Classify this cell by malaria status.
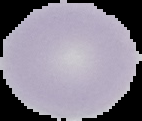
Uninfected.

Image is 142×121 pixels. From a thin blood smear. Cell region segmented out of the field of view; the surrounding area is masked to black.